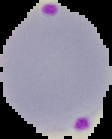
result = Plasmodium parasites identified
image type = segmented cell region with the area outside set to black
image size = 112×139 pixels
preparation = thin blood film